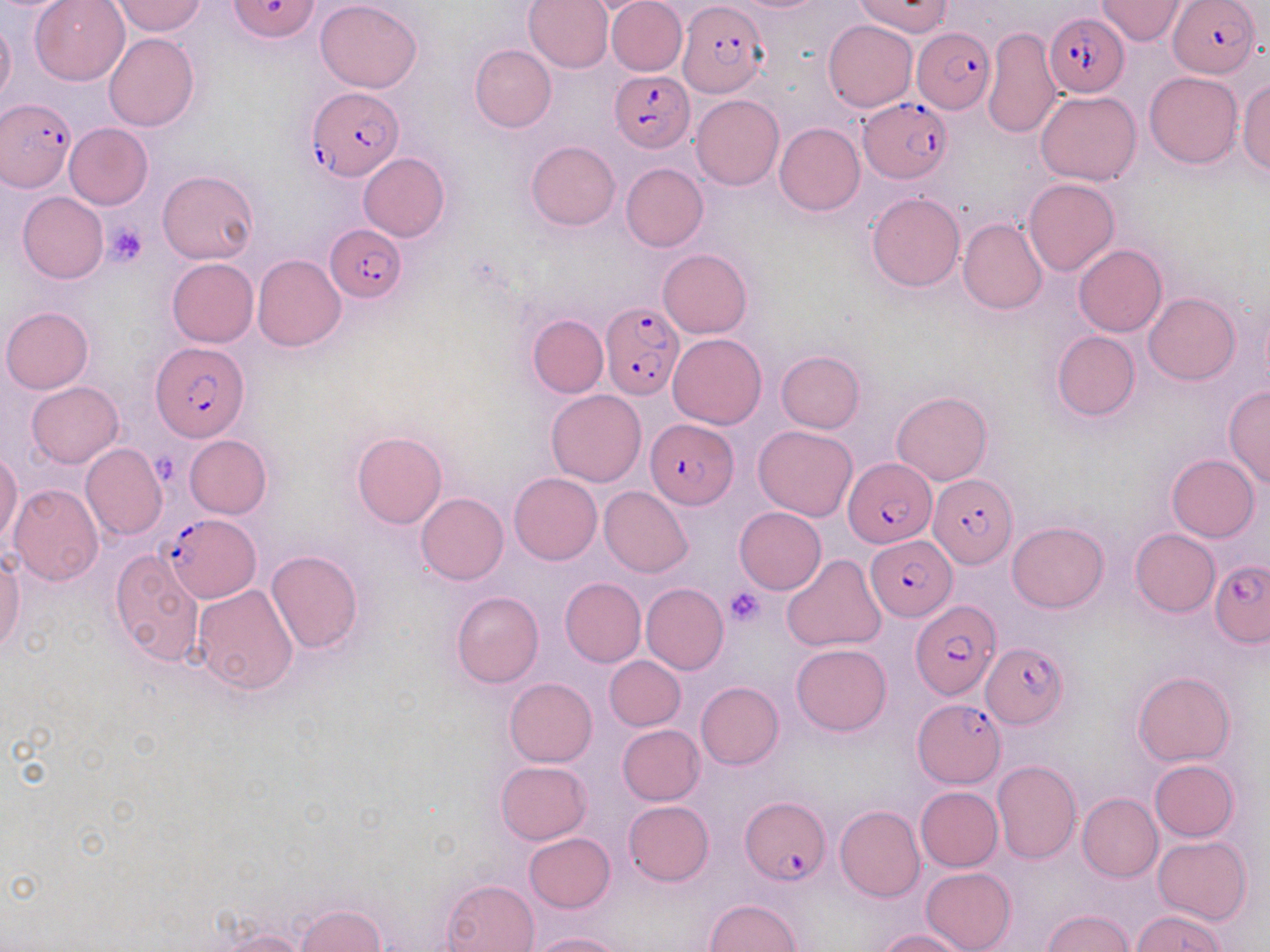
Summary:
  - Coordinate format: approximate bounding boxes as [x1, y1, x2, y2] in pixels
  - Uninfected red blood cell locations: [29, 0, 130, 85], [110, 0, 206, 36], [315, 0, 421, 93], [522, 0, 613, 73], [606, 0, 687, 76], [1096, 0, 1186, 43], [0, 17, 16, 109], [823, 20, 917, 111], [983, 26, 1063, 136], [104, 33, 199, 132], [469, 44, 556, 132], [1145, 72, 1242, 169], [1237, 80, 1270, 176], [1036, 90, 1142, 185], [691, 94, 783, 191], [64, 123, 152, 210], [774, 123, 864, 215], [526, 140, 620, 230], [358, 153, 450, 241], [621, 162, 708, 251], [158, 170, 261, 264], [1024, 179, 1119, 276], [17, 192, 109, 283], [868, 193, 965, 291], [959, 218, 1047, 314], [1073, 244, 1167, 337], [658, 248, 751, 339], [252, 254, 345, 351], [166, 257, 258, 347], [1143, 292, 1240, 384], [1, 305, 94, 392], [527, 314, 608, 398], [1051, 331, 1141, 421], [667, 333, 767, 429], [776, 350, 865, 434], [26, 381, 123, 467], [1224, 385, 1270, 489], [546, 389, 645, 487], [891, 392, 992, 485], [753, 425, 857, 520], [352, 430, 446, 529], [184, 434, 272, 518], [81, 443, 166, 541], [0, 451, 22, 545], [26, 454, 160, 560], [1167, 454, 1260, 542], [509, 472, 601, 565], [8, 484, 104, 587], [600, 486, 693, 577], [416, 493, 509, 585], [734, 507, 826, 594], [1007, 521, 1108, 612], [1130, 529, 1219, 616], [0, 549, 25, 656], [109, 549, 204, 666], [265, 550, 363, 655], [781, 554, 887, 652], [560, 578, 647, 667], [641, 583, 729, 674], [192, 584, 298, 694], [451, 591, 543, 688], [791, 644, 892, 736], [605, 656, 685, 731], [1133, 671, 1235, 766], [504, 677, 597, 766], [696, 681, 784, 769], [618, 725, 704, 804], [1149, 759, 1240, 842], [495, 760, 592, 845], [991, 760, 1081, 865], [915, 786, 1003, 872], [1077, 793, 1162, 882], [623, 801, 714, 885], [835, 805, 925, 902], [524, 833, 615, 912], [1153, 835, 1252, 926], [921, 866, 1016, 952], [442, 878, 538, 952], [706, 899, 801, 951], [295, 905, 387, 951], [1042, 909, 1135, 952], [1131, 910, 1227, 951], [212, 928, 310, 952], [877, 928, 968, 951], [528, 932, 626, 952]
  - Plasmodium falciparum-infected red blood cell locations: [229, 0, 321, 42], [1169, 1, 1261, 78], [677, 3, 768, 97], [1044, 12, 1130, 96], [912, 26, 995, 113], [609, 71, 695, 152], [306, 88, 402, 182], [858, 97, 951, 183], [1, 99, 75, 191], [327, 225, 407, 303], [602, 300, 685, 398], [150, 343, 250, 442], [644, 418, 737, 508], [843, 457, 936, 547], [928, 475, 1015, 570], [161, 511, 261, 601], [866, 536, 955, 621], [1210, 560, 1270, 647], [909, 599, 1000, 702], [980, 641, 1069, 730], [914, 697, 1005, 789], [740, 798, 831, 885]
  - Platelet locations: [105, 224, 148, 267], [724, 587, 765, 627]
  - Slide-level diagnosis: Plasmodium falciparum
  - Image size: 1270×952 pixels
  - Magnification: 1000x
  - Field of view: one of a larger specimen
  - Modality: light microscopy
  - Preparation: thin blood smear
  - Stain: May-Grünwald-Giemsa